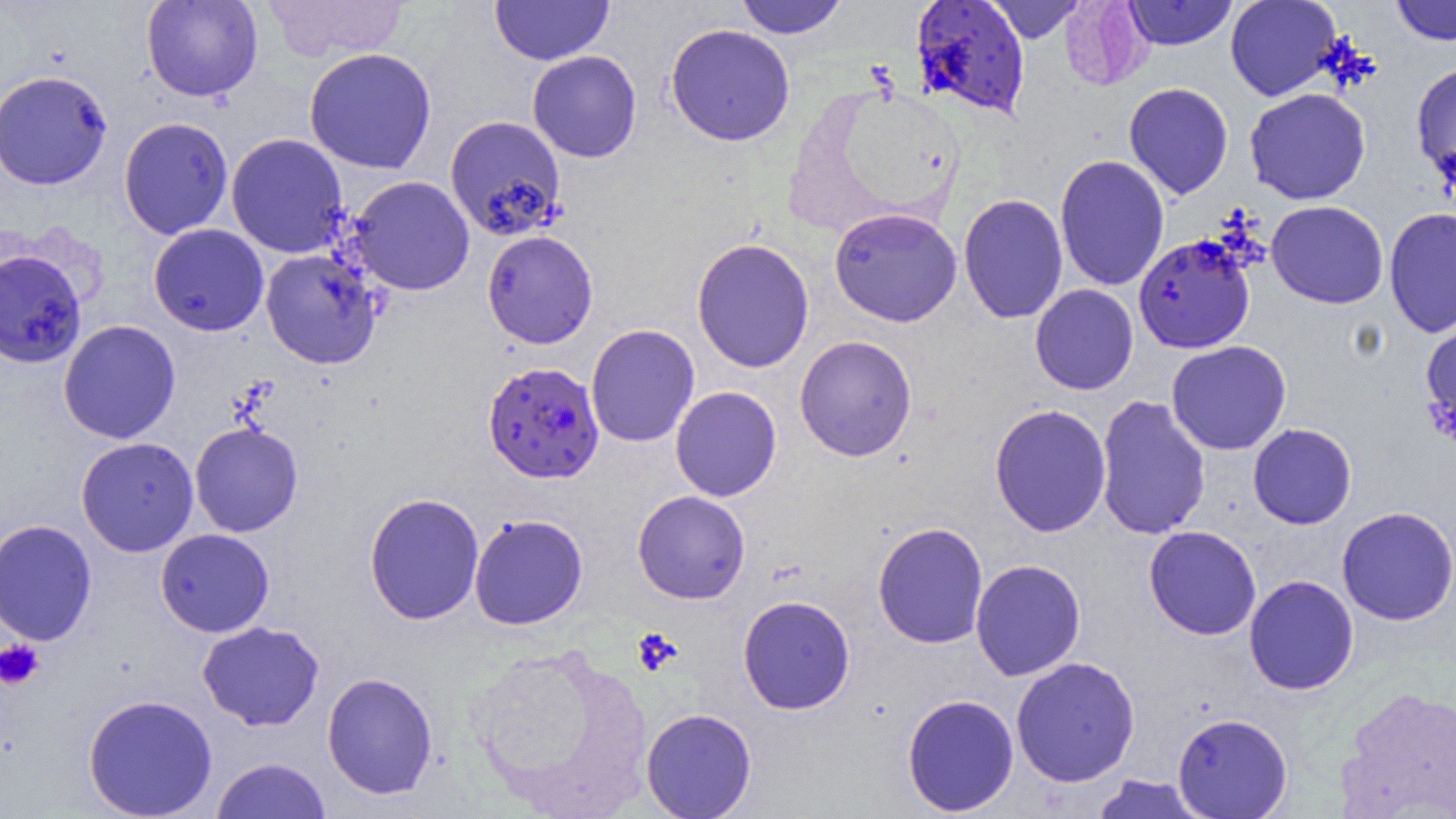
Summary:
  - Coordinate format: approximate bounding boxes as named x1/y1/x2/y2 corners in pixels
  - Uninfected red blood cell locations: (x1=141, y1=0, x2=263, y2=102), (x1=262, y1=0, x2=409, y2=62), (x1=489, y1=0, x2=614, y2=65), (x1=734, y1=0, x2=848, y2=38), (x1=986, y1=0, x2=1087, y2=43), (x1=1059, y1=0, x2=1152, y2=90), (x1=1123, y1=0, x2=1237, y2=50), (x1=1225, y1=0, x2=1342, y2=101), (x1=1391, y1=0, x2=1456, y2=45), (x1=665, y1=23, x2=796, y2=146), (x1=304, y1=48, x2=437, y2=174), (x1=527, y1=50, x2=642, y2=163), (x1=1411, y1=61, x2=1456, y2=189), (x1=0, y1=69, x2=112, y2=190), (x1=1124, y1=82, x2=1234, y2=200), (x1=1245, y1=88, x2=1371, y2=205), (x1=445, y1=114, x2=566, y2=239), (x1=118, y1=117, x2=233, y2=239), (x1=226, y1=133, x2=349, y2=258), (x1=1054, y1=154, x2=1170, y2=291), (x1=349, y1=175, x2=475, y2=296), (x1=958, y1=193, x2=1068, y2=324), (x1=1266, y1=200, x2=1389, y2=309), (x1=829, y1=207, x2=962, y2=327), (x1=1384, y1=208, x2=1456, y2=338), (x1=148, y1=223, x2=269, y2=336), (x1=482, y1=229, x2=598, y2=349), (x1=692, y1=238, x2=814, y2=373), (x1=0, y1=249, x2=87, y2=368), (x1=261, y1=249, x2=382, y2=369), (x1=1030, y1=284, x2=1139, y2=395), (x1=1421, y1=319, x2=1456, y2=442), (x1=58, y1=320, x2=181, y2=443), (x1=585, y1=323, x2=700, y2=447), (x1=795, y1=335, x2=917, y2=461), (x1=1166, y1=340, x2=1292, y2=455), (x1=670, y1=386, x2=782, y2=501), (x1=1095, y1=394, x2=1211, y2=541), (x1=989, y1=403, x2=1111, y2=537), (x1=190, y1=422, x2=303, y2=537), (x1=1248, y1=423, x2=1357, y2=529), (x1=76, y1=437, x2=198, y2=557), (x1=633, y1=490, x2=750, y2=604), (x1=364, y1=492, x2=484, y2=625), (x1=1336, y1=507, x2=1456, y2=625), (x1=469, y1=513, x2=588, y2=630), (x1=0, y1=520, x2=97, y2=646), (x1=873, y1=521, x2=989, y2=649), (x1=1144, y1=525, x2=1262, y2=640), (x1=156, y1=528, x2=274, y2=637), (x1=970, y1=559, x2=1086, y2=681), (x1=1244, y1=575, x2=1359, y2=695), (x1=738, y1=595, x2=855, y2=715), (x1=197, y1=621, x2=324, y2=731), (x1=464, y1=643, x2=650, y2=815), (x1=1010, y1=656, x2=1140, y2=787), (x1=322, y1=672, x2=438, y2=799), (x1=1336, y1=686, x2=1456, y2=817), (x1=83, y1=693, x2=218, y2=819), (x1=901, y1=693, x2=1019, y2=816), (x1=641, y1=708, x2=756, y2=818), (x1=1172, y1=712, x2=1293, y2=818), (x1=211, y1=757, x2=331, y2=819), (x1=1090, y1=774, x2=1210, y2=818)
  - Platelet locations: (x1=632, y1=628, x2=681, y2=675), (x1=0, y1=639, x2=44, y2=690)
  - Plasmodium falciparum-infected red blood cell locations: (x1=910, y1=1, x2=1031, y2=119), (x1=1133, y1=233, x2=1256, y2=354), (x1=483, y1=361, x2=604, y2=484)
  - Slide-level diagnosis: Plasmodium falciparum
  - Field of view: single
  - Modality: optical microscopy
  - Magnification: 1000x
  - Image size: 1456×819 pixels
  - Preparation: thin blood film